Name the parasite shown.
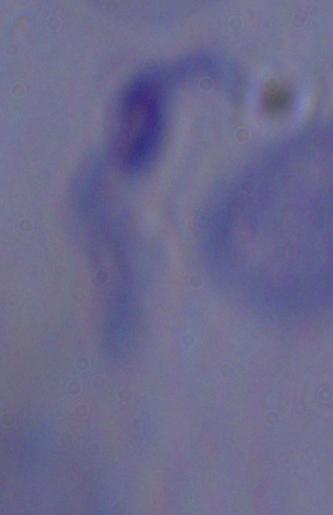
This is a trypanosome.

magnification = 1000x
modality = photomicrograph